Name the blood parasite species.
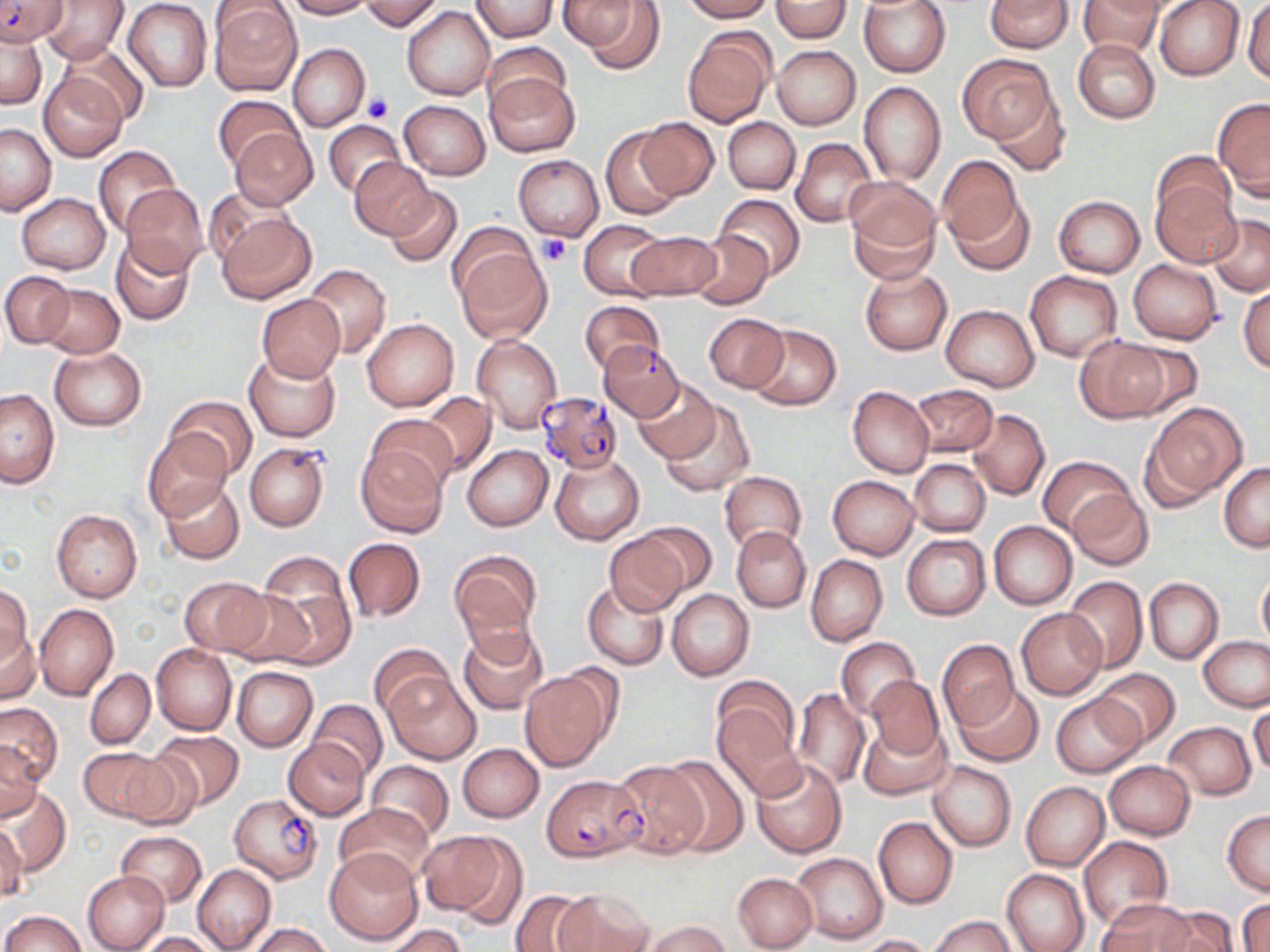

Plasmodium falciparum.

modality = optical microscopy
Plasmodium falciparum-infected red blood cell locations = approximate bounding boxes as (x1,y1)-(x2,y2) corner pairs in pixels: (0,0)-(66,46), (598,341)-(683,421), (536,391)-(623,472), (543,774)-(647,862), (230,794)-(322,882)
uninfected red blood cell locations = approximate bounding boxes as (x1,y1)-(x2,y2) corner pairs in pixels: (123,0)-(211,92), (281,0)-(371,18), (359,0)-(444,32), (681,0)-(772,22), (771,0)-(852,41), (858,0)-(952,78), (984,0)-(1072,52), (1153,0)-(1247,81), (1243,0)-(1270,84), (38,1)-(128,64), (469,1)-(558,40), (1079,1)-(1164,59), (209,2)-(302,95), (572,2)-(662,74), (402,7)-(493,99), (0,29)-(46,110), (683,30)-(775,126), (1072,39)-(1159,123), (58,43)-(149,126), (289,43)-(369,132), (482,43)-(572,116), (771,45)-(861,129), (958,54)-(1059,149), (484,70)-(582,158), (39,72)-(128,162), (858,81)-(945,184), (990,91)-(1071,177), (213,94)-(302,173), (1213,98)-(1270,200), (400,99)-(489,179), (722,117)-(800,193), (633,118)-(719,200), (322,119)-(407,197), (0,123)-(55,215), (230,128)-(317,209), (601,128)-(684,220), (790,138)-(876,228), (93,146)-(179,236), (1152,152)-(1237,228), (513,153)-(604,242), (935,156)-(1026,247), (349,157)-(436,240), (843,178)-(941,281), (1151,180)-(1240,267), (121,185)-(209,277), (384,186)-(463,268), (201,189)-(291,271), (946,190)-(1035,276), (18,193)-(109,274), (714,194)-(805,279), (1054,196)-(1144,277), (217,211)-(316,304), (1208,214)-(1270,296), (577,219)-(667,300), (626,230)-(722,301), (689,233)-(772,307), (452,234)-(550,343), (110,236)-(197,327), (1129,259)-(1222,343), (301,263)-(390,358), (860,267)-(952,356), (1,270)-(74,348), (1025,270)-(1122,361), (37,283)-(125,357), (1239,285)-(1270,373), (257,294)-(345,382), (578,299)-(664,375), (940,304)-(1039,391), (703,313)-(789,392), (363,318)-(458,411), (747,324)-(841,411), (471,335)-(562,434), (1074,336)-(1172,421), (1113,338)-(1203,419), (48,345)-(148,431), (243,349)-(342,441), (632,377)-(720,464), (911,383)-(998,457), (848,386)-(933,478), (0,387)-(60,487), (419,391)-(496,478), (167,395)-(256,480), (659,398)-(755,498), (1144,404)-(1245,503), (967,408)-(1050,501), (366,412)-(456,493), (144,427)-(233,522), (244,442)-(329,531), (355,443)-(447,536), (463,444)-(552,531), (550,454)-(644,545), (1038,455)-(1137,540), (909,459)-(990,537), (1218,463)-(1270,551), (720,471)-(807,553), (828,475)-(921,560), (159,479)-(245,566), (1069,489)-(1152,570), (51,509)-(142,602), (632,520)-(718,600), (989,521)-(1077,610), (732,526)-(811,612), (605,531)-(690,617), (902,534)-(990,620), (342,537)-(425,622), (448,550)-(542,649), (256,552)-(355,662), (805,554)-(888,646), (1257,570)-(1270,648), (181,576)-(268,656), (1063,576)-(1148,672), (1145,578)-(1223,665), (582,581)-(669,669), (0,583)-(31,672), (223,587)-(316,668), (666,589)-(754,680), (34,604)-(118,699), (1017,608)-(1106,699), (457,625)-(549,715), (1,626)-(40,704), (1199,636)-(1270,711), (835,637)-(920,718), (936,639)-(1020,730), (151,644)-(236,734), (369,644)-(453,721), (231,666)-(317,751), (1094,668)-(1180,748), (85,669)-(155,748), (386,669)-(482,764), (518,670)-(614,772), (866,676)-(943,759), (953,683)-(1042,767), (711,687)-(802,793), (791,688)-(871,790), (1051,693)-(1145,777), (308,699)-(387,780), (1249,700)-(1270,780), (0,703)-(62,788), (859,718)-(949,800), (1165,721)-(1255,799), (151,731)-(245,809), (283,738)-(370,820), (0,742)-(42,821), (457,743)-(544,821), (79,747)-(173,823), (116,749)-(206,830), (661,754)-(750,857), (751,757)-(847,857), (1104,759)-(1195,840), (367,760)-(453,841), (608,760)-(711,860), (928,760)-(1016,851), (1021,781)-(1109,870), (4,788)-(70,875), (334,802)-(434,885), (1223,810)-(1270,894), (873,816)-(958,908), (0,825)-(26,900), (116,831)-(206,906), (421,831)-(524,923), (1078,836)-(1173,931), (325,848)-(423,945), (791,852)-(887,945), (192,864)-(277,952), (1002,869)-(1089,952), (82,871)-(170,952), (733,873)-(817,951), (551,887)-(659,952), (511,889)-(594,952), (1237,898)-(1269,952), (1098,899)-(1195,951), (1155,906)-(1239,952), (2,910)-(84,952), (930,915)-(1017,952), (638,919)-(731,952), (246,923)-(332,952), (386,924)-(465,952), (141,932)-(220,952), (857,934)-(935,952)
stain = May-Grünwald-Giemsa
image size = 1270×952 pixels
field of view = one of a larger specimen
platelet locations = approximate bounding boxes as (x1,y1)-(x2,y2) corner pairs in pixels: (365,93)-(393,122), (538,234)-(569,266)
preparation = thin blood smear
magnification = 1000x